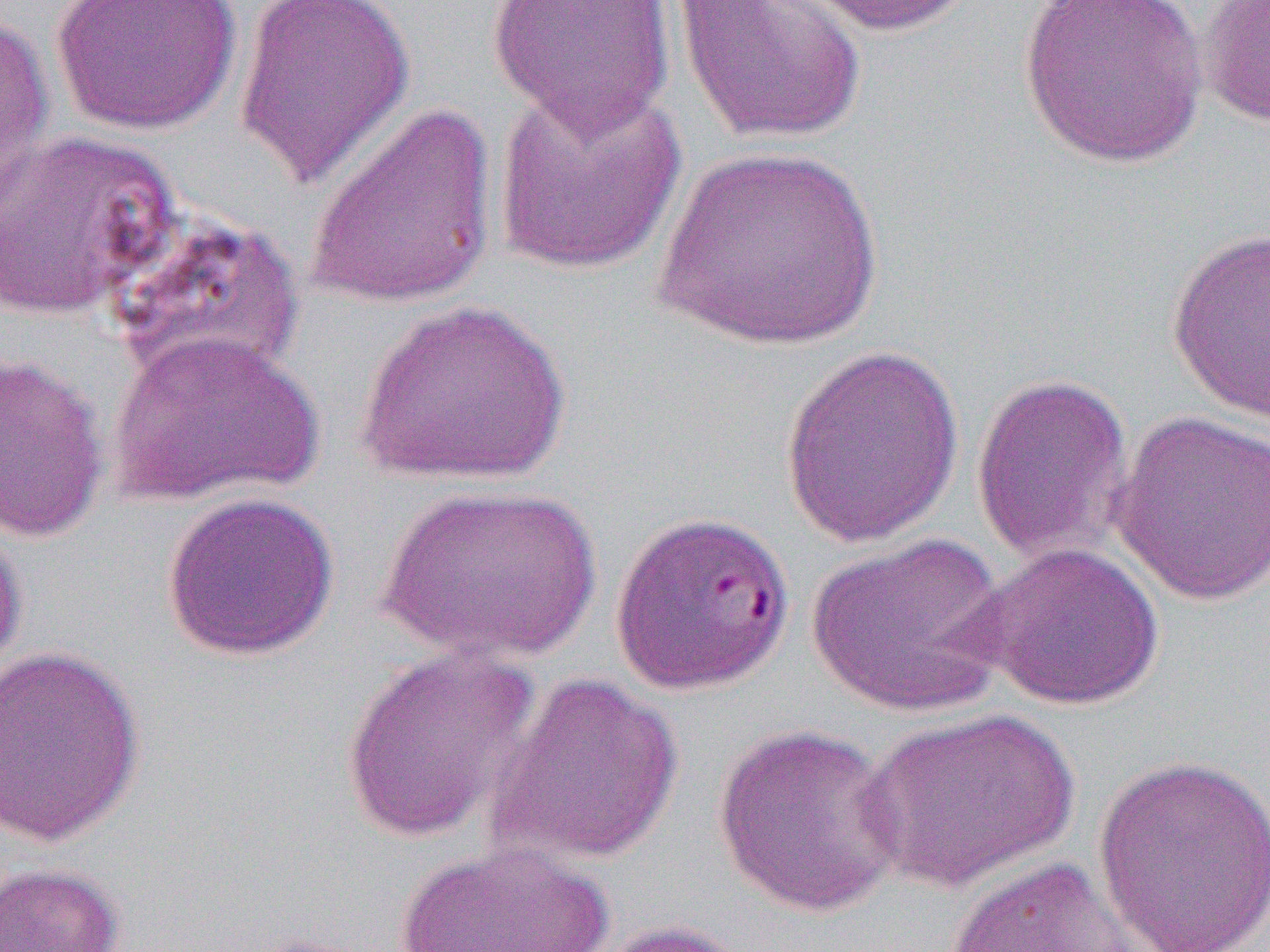

Approximate bounding boxes as (x1, y1, x2, y2) in pixels. Uninfected red blood cell locations: (49, 0, 243, 136), (233, 0, 416, 189), (485, 0, 677, 138), (673, 0, 869, 147), (784, 0, 978, 37), (1017, 0, 1211, 169), (1199, 1, 1270, 128), (1, 9, 55, 224), (493, 81, 689, 277), (305, 101, 501, 310), (0, 129, 181, 323), (654, 144, 884, 351), (110, 212, 305, 386), (1166, 226, 1270, 423), (355, 298, 573, 487), (108, 330, 323, 507), (778, 343, 966, 549), (0, 350, 111, 544), (970, 371, 1135, 565), (1108, 409, 1270, 607), (376, 483, 601, 663), (161, 491, 340, 662), (0, 509, 27, 683), (805, 532, 1012, 719), (975, 541, 1165, 711), (0, 645, 146, 847), (339, 645, 540, 844), (487, 672, 685, 867), (859, 708, 1082, 894), (712, 722, 908, 918), (1092, 753, 1270, 950), (393, 841, 617, 952), (942, 854, 1161, 952), (0, 862, 125, 952), (588, 918, 758, 952). Slide-level diagnosis: Plasmodium falciparum. Thin blood smear. Optical microscopy. Single field of view. Image is 1270×952 pixels. Captured at 1000x magnification.